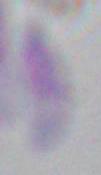
Photomicrograph. Captured at 1000x magnification. Toxoplasma gondii is seen.